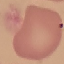
{
  "result": "no malaria parasites seen",
  "stain": "Giemsa",
  "capture": "smartphone through the microscope eyepiece",
  "image_type": "automatically extracted cell patch, resized to 64 × 64 pixels",
  "preparation": "thin smear"
}